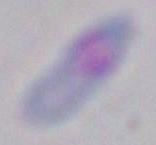
magnification = 1000x
identification = Toxoplasma gondii
modality = micrograph